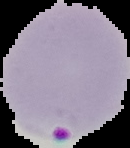
image type = segmented cell region on a black background
image size = 130×148 pixels
preparation = thin blood film
result = malaria parasites detected